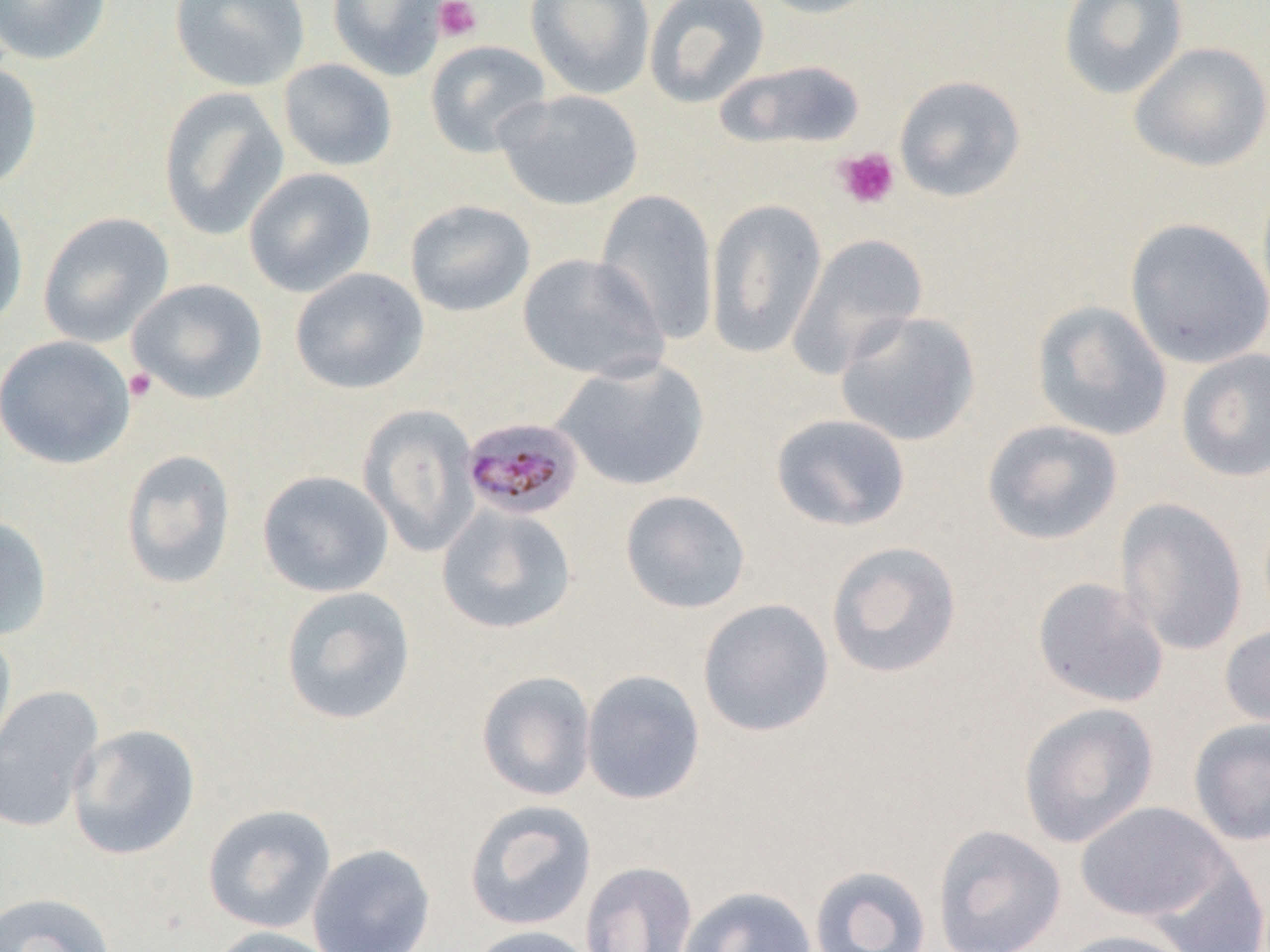
Summary:
  - Coordinate format: approximate bounding boxes as [x1, y1, x2, y2] in pixels
  - Uninfected red blood cell locations: [0, 0, 112, 66], [169, 0, 311, 91], [327, 0, 448, 81], [525, 0, 655, 100], [644, 0, 770, 108], [753, 0, 886, 19], [1058, 0, 1189, 100], [424, 39, 552, 158], [1128, 41, 1270, 172], [277, 58, 398, 172], [716, 59, 865, 151], [0, 60, 43, 192], [893, 74, 1026, 202], [157, 87, 291, 240], [495, 89, 644, 211], [243, 167, 377, 297], [1256, 171, 1270, 319], [594, 189, 720, 344], [0, 191, 29, 334], [705, 198, 827, 357], [404, 199, 536, 317], [38, 212, 174, 347], [1124, 217, 1270, 369], [787, 233, 928, 379], [517, 252, 668, 382], [289, 267, 428, 395], [127, 278, 268, 404], [1031, 300, 1173, 441], [835, 310, 981, 446], [0, 334, 136, 469], [1176, 348, 1270, 482], [552, 356, 711, 492], [358, 404, 481, 558], [770, 413, 912, 532], [982, 419, 1123, 545], [120, 448, 237, 590], [257, 470, 394, 598], [620, 489, 751, 614], [1116, 497, 1248, 657], [437, 503, 577, 635], [0, 514, 53, 642], [826, 541, 962, 679], [1032, 577, 1169, 709], [280, 585, 416, 725], [697, 598, 834, 738], [1219, 621, 1270, 732], [0, 627, 17, 765], [581, 669, 706, 805], [476, 670, 597, 801], [0, 684, 105, 834], [1017, 701, 1160, 848], [1188, 716, 1270, 846], [67, 723, 201, 861], [463, 799, 597, 932], [1075, 801, 1233, 923], [202, 804, 336, 934], [932, 824, 1067, 952], [307, 843, 436, 952], [1143, 850, 1270, 952], [579, 860, 698, 952], [808, 864, 933, 952], [678, 885, 817, 952], [0, 891, 117, 952], [466, 924, 601, 952], [203, 925, 346, 952], [1053, 928, 1197, 952]
  - Platelet locations: [434, 0, 482, 43], [834, 147, 900, 210], [124, 369, 157, 403]
  - Plasmodium malariae-infected red blood cell locations: [461, 416, 585, 521]
  - Slide-level diagnosis: Plasmodium malariae
  - Field of view: one of a larger specimen
  - Image size: 1270×952 pixels
  - Preparation: thin blood film
  - Modality: light microscopy
  - Magnification: 1000x